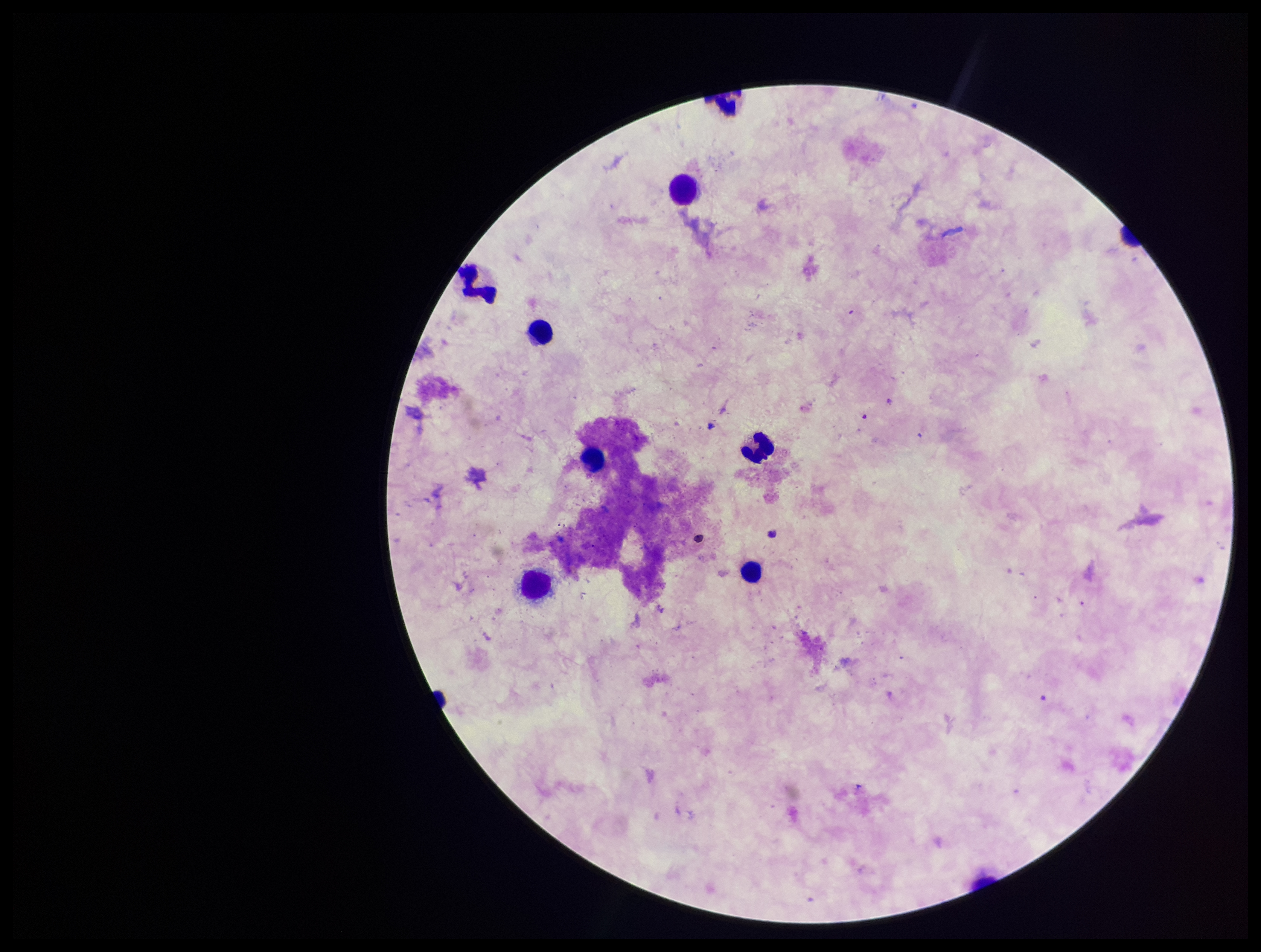
Summary:
  - Stain: Giemsa
  - Parasite count: 0
  - Image size: 1261×952 pixels
  - Plasmodium parasites: none seen
  - Capture: smartphone photograph through the microscope eyepiece
  - Preparation: thick smear
  - Field of view: single
  - Leukocyte count: 9
  - Patient malaria status: negative